Outline each blood parasite and name the species.
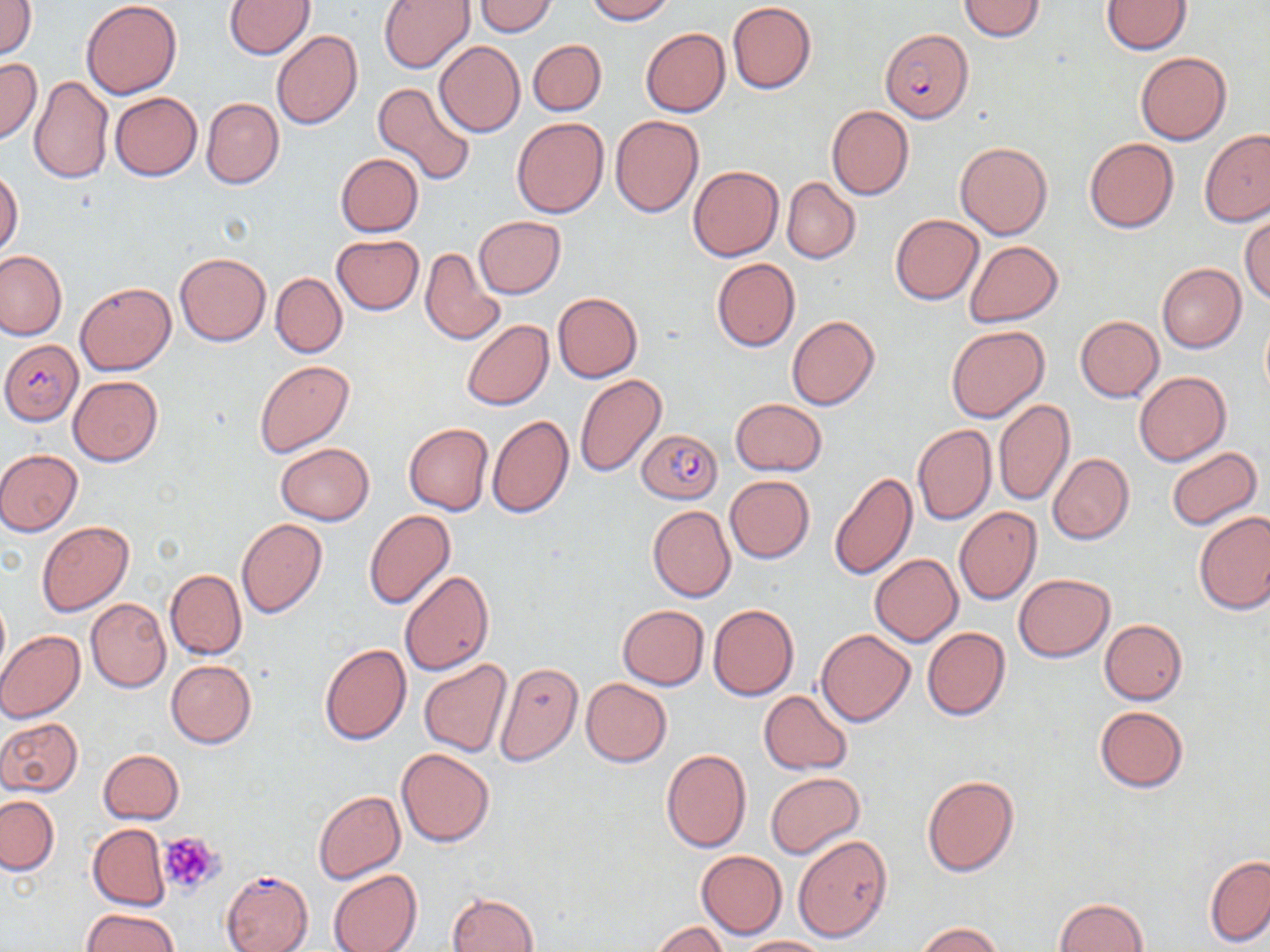

Approximate bounding boxes as (x1, y1, x2, y2) in pixels.
Plasmodium falciparum-infected red blood cells: (880, 28, 972, 122), (1, 341, 81, 424), (638, 426, 722, 501), (221, 871, 313, 952).
No Plasmodium ovale, Plasmodium malariae, Plasmodium vivax, Babesia divergens, or Trypanosoma brucei observed.

Summary:
  - Platelet locations: (157, 831, 227, 896)
  - Uninfected red blood cell locations: (224, 0, 316, 59), (378, 0, 474, 72), (475, 0, 557, 36), (584, 0, 675, 23), (1, 1, 36, 60), (958, 1, 1046, 41), (1101, 1, 1192, 54), (82, 2, 181, 99), (727, 2, 816, 93), (640, 28, 731, 117), (272, 31, 363, 129), (529, 39, 606, 116), (435, 42, 525, 137), (1136, 52, 1231, 145), (0, 57, 41, 144), (28, 76, 113, 184), (371, 81, 476, 186), (110, 92, 202, 181), (201, 97, 284, 188), (826, 105, 914, 200), (610, 115, 704, 217), (511, 117, 609, 218), (1200, 129, 1270, 226), (1084, 137, 1179, 233), (955, 141, 1052, 240), (335, 153, 423, 237), (688, 165, 783, 261), (0, 168, 23, 259), (782, 177, 860, 264), (890, 214, 984, 304), (475, 215, 565, 298), (1241, 215, 1269, 305), (331, 235, 423, 314), (963, 240, 1062, 326), (419, 247, 507, 346), (0, 250, 67, 340), (175, 252, 271, 345), (712, 258, 800, 352), (1156, 263, 1246, 352), (271, 272, 348, 357), (75, 282, 175, 375), (553, 293, 643, 382), (1075, 315, 1163, 402), (786, 316, 879, 410), (1261, 318, 1270, 400), (462, 320, 553, 410), (945, 325, 1048, 424), (255, 361, 354, 458), (1134, 370, 1231, 467), (575, 373, 667, 478), (68, 374, 163, 466), (730, 398, 827, 476), (994, 398, 1075, 506), (487, 415, 574, 518), (404, 423, 493, 515), (912, 424, 996, 525), (275, 442, 375, 525), (1166, 446, 1261, 531), (0, 449, 82, 535), (1048, 452, 1134, 545), (829, 472, 918, 581), (724, 475, 814, 563), (647, 505, 736, 602), (954, 507, 1042, 605), (364, 510, 455, 609), (1193, 510, 1270, 614), (237, 518, 327, 618), (37, 521, 134, 615), (870, 554, 963, 645), (165, 569, 246, 661), (399, 570, 493, 675), (1014, 573, 1114, 662), (86, 598, 170, 692), (0, 600, 10, 677), (616, 604, 709, 690), (709, 604, 799, 701), (1100, 619, 1188, 705), (922, 626, 1011, 721), (816, 628, 914, 726), (0, 629, 85, 722), (319, 643, 412, 745), (165, 659, 257, 748), (418, 660, 513, 757), (493, 662, 585, 766), (581, 677, 672, 767), (759, 690, 853, 774), (1094, 706, 1189, 793), (0, 718, 83, 796), (397, 748, 495, 847), (661, 749, 751, 852), (98, 750, 184, 825), (765, 772, 864, 859), (922, 775, 1019, 876), (312, 790, 406, 883), (1, 795, 58, 874), (88, 824, 170, 911), (793, 834, 893, 941), (696, 850, 787, 938), (1205, 854, 1270, 948), (328, 869, 422, 952), (448, 891, 538, 952), (1055, 897, 1148, 952), (82, 909, 178, 952), (653, 921, 729, 952), (914, 922, 1006, 952), (733, 935, 831, 951)
  - Slide-level diagnosis: Plasmodium falciparum
  - Field of view: one of a larger specimen
  - Modality: light microscopy
  - Magnification: 1000x
  - Image size: 1270×952 pixels
  - Stain: May-Grünwald-Giemsa
  - Preparation: thin blood film